Assess this cell for malaria.
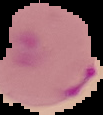

Parasitized.

Image is 103×115 pixels. From a thin blood film. Cell region segmented out of the field of view; the surrounding area is masked to black.